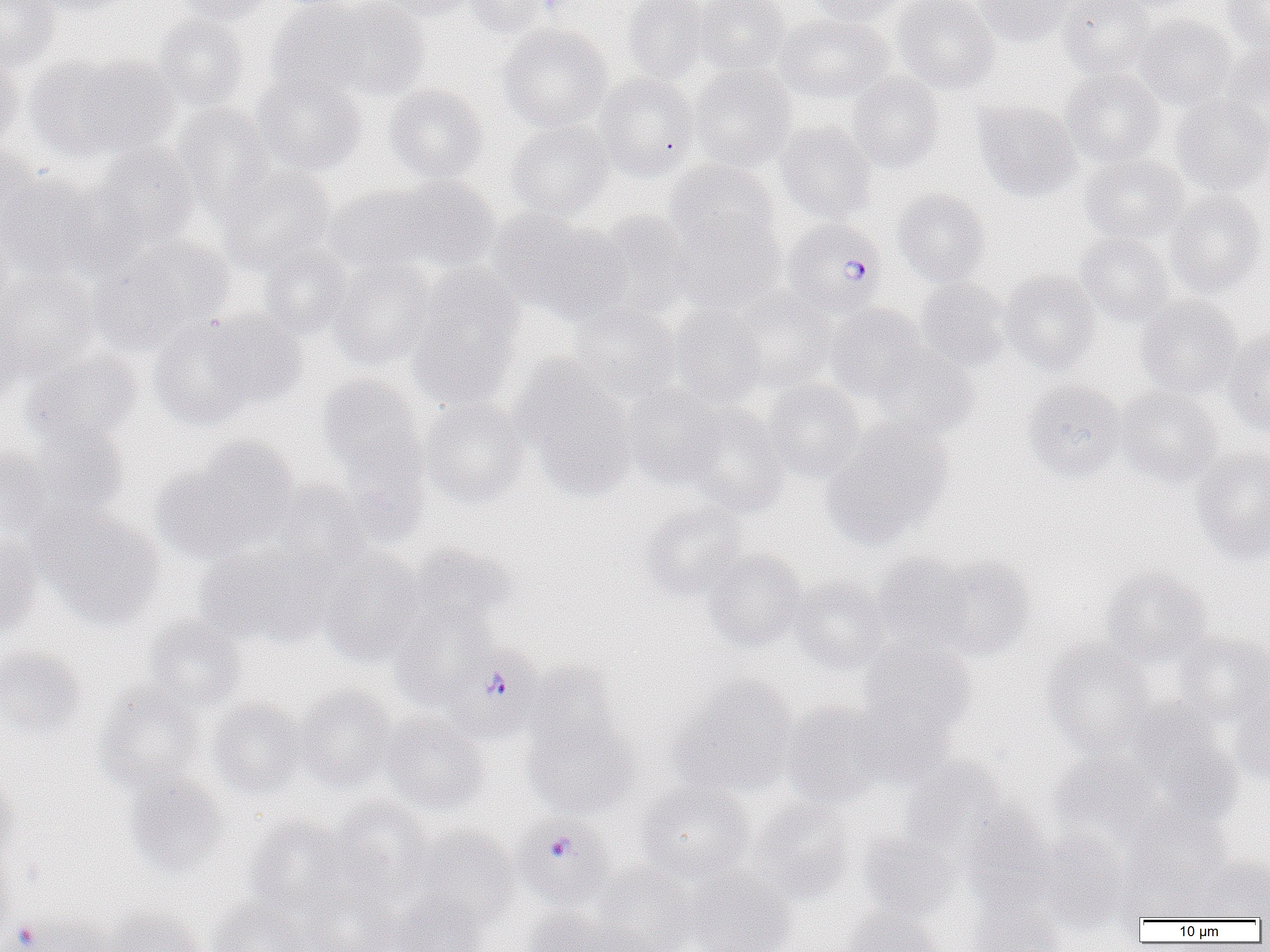
Summary:
  - Coordinate format: approximate bounding boxes as named x1/y1/x2/y2 corners in pixels
  - Plasmodium falciparum-infected red blood cell locations: (x1=782, y1=218, x2=886, y2=318), (x1=437, y1=637, x2=549, y2=743), (x1=518, y1=817, x2=610, y2=904)
  - Platelet locations: (x1=10, y1=919, x2=42, y2=951)
  - Uninfected red blood cell locations: (x1=0, y1=0, x2=61, y2=72), (x1=29, y1=0, x2=143, y2=17), (x1=173, y1=0, x2=276, y2=24), (x1=383, y1=0, x2=478, y2=20), (x1=465, y1=0, x2=555, y2=37), (x1=621, y1=0, x2=709, y2=82), (x1=694, y1=0, x2=789, y2=75), (x1=804, y1=0, x2=909, y2=24), (x1=892, y1=0, x2=1000, y2=94), (x1=973, y1=0, x2=1075, y2=47), (x1=1058, y1=0, x2=1156, y2=79), (x1=1221, y1=0, x2=1270, y2=49), (x1=266, y1=1, x2=375, y2=101), (x1=321, y1=1, x2=430, y2=102), (x1=775, y1=12, x2=892, y2=104), (x1=151, y1=14, x2=249, y2=112), (x1=1134, y1=14, x2=1237, y2=109), (x1=498, y1=23, x2=612, y2=131), (x1=1220, y1=39, x2=1270, y2=139), (x1=0, y1=53, x2=25, y2=153), (x1=39, y1=54, x2=183, y2=160), (x1=690, y1=65, x2=796, y2=171), (x1=1060, y1=69, x2=1166, y2=168), (x1=595, y1=72, x2=699, y2=180), (x1=251, y1=73, x2=368, y2=176), (x1=846, y1=73, x2=944, y2=171), (x1=383, y1=83, x2=488, y2=183), (x1=1170, y1=93, x2=1270, y2=194), (x1=973, y1=100, x2=1081, y2=201), (x1=174, y1=103, x2=276, y2=216), (x1=507, y1=120, x2=613, y2=220), (x1=775, y1=120, x2=878, y2=223), (x1=0, y1=144, x2=42, y2=237), (x1=92, y1=144, x2=199, y2=249), (x1=1079, y1=153, x2=1188, y2=244), (x1=665, y1=161, x2=779, y2=255), (x1=217, y1=165, x2=337, y2=276), (x1=0, y1=171, x2=103, y2=277), (x1=392, y1=175, x2=500, y2=272), (x1=326, y1=183, x2=442, y2=275), (x1=893, y1=188, x2=990, y2=287), (x1=1164, y1=190, x2=1268, y2=297), (x1=588, y1=210, x2=694, y2=321), (x1=670, y1=211, x2=783, y2=312), (x1=495, y1=213, x2=627, y2=321), (x1=1074, y1=231, x2=1176, y2=326), (x1=94, y1=237, x2=230, y2=348), (x1=257, y1=242, x2=354, y2=339), (x1=327, y1=259, x2=437, y2=369), (x1=0, y1=267, x2=98, y2=381), (x1=1000, y1=270, x2=1101, y2=373), (x1=407, y1=275, x2=522, y2=409), (x1=915, y1=279, x2=1011, y2=371), (x1=725, y1=289, x2=835, y2=392), (x1=1134, y1=296, x2=1242, y2=398), (x1=569, y1=303, x2=681, y2=403), (x1=667, y1=304, x2=766, y2=409), (x1=824, y1=304, x2=927, y2=400), (x1=0, y1=309, x2=23, y2=413), (x1=203, y1=309, x2=306, y2=408), (x1=148, y1=320, x2=258, y2=430), (x1=1223, y1=327, x2=1270, y2=437), (x1=872, y1=345, x2=979, y2=439), (x1=21, y1=350, x2=142, y2=452), (x1=517, y1=366, x2=638, y2=497), (x1=316, y1=374, x2=425, y2=482), (x1=763, y1=379, x2=867, y2=482), (x1=1023, y1=379, x2=1126, y2=481), (x1=622, y1=384, x2=728, y2=488), (x1=1115, y1=385, x2=1222, y2=485), (x1=420, y1=397, x2=530, y2=507), (x1=681, y1=405, x2=790, y2=517), (x1=822, y1=421, x2=952, y2=548), (x1=20, y1=424, x2=130, y2=527), (x1=156, y1=441, x2=298, y2=564), (x1=0, y1=445, x2=54, y2=538), (x1=1191, y1=447, x2=1270, y2=565), (x1=268, y1=480, x2=371, y2=577), (x1=640, y1=501, x2=748, y2=599), (x1=40, y1=511, x2=165, y2=629), (x1=0, y1=530, x2=44, y2=639), (x1=197, y1=541, x2=332, y2=647), (x1=410, y1=544, x2=516, y2=631), (x1=703, y1=548, x2=809, y2=651), (x1=318, y1=549, x2=430, y2=666), (x1=874, y1=552, x2=971, y2=646), (x1=925, y1=556, x2=1034, y2=660), (x1=1099, y1=566, x2=1211, y2=667), (x1=791, y1=574, x2=890, y2=672), (x1=391, y1=608, x2=494, y2=707), (x1=142, y1=614, x2=247, y2=712), (x1=1173, y1=631, x2=1270, y2=726), (x1=859, y1=640, x2=975, y2=739), (x1=1041, y1=641, x2=1157, y2=756), (x1=0, y1=645, x2=87, y2=743), (x1=526, y1=663, x2=622, y2=755), (x1=669, y1=675, x2=799, y2=800), (x1=95, y1=681, x2=207, y2=794), (x1=294, y1=685, x2=396, y2=791), (x1=1233, y1=693, x2=1270, y2=786), (x1=207, y1=698, x2=309, y2=799), (x1=850, y1=699, x2=957, y2=789), (x1=781, y1=701, x2=888, y2=808), (x1=1118, y1=705, x2=1241, y2=829), (x1=521, y1=708, x2=641, y2=819), (x1=378, y1=712, x2=490, y2=814), (x1=1049, y1=752, x2=1162, y2=848), (x1=902, y1=757, x2=1019, y2=862), (x1=125, y1=771, x2=230, y2=878), (x1=0, y1=772, x2=19, y2=872), (x1=637, y1=780, x2=756, y2=882), (x1=326, y1=797, x2=436, y2=902), (x1=748, y1=800, x2=857, y2=903), (x1=1127, y1=805, x2=1234, y2=901), (x1=960, y1=807, x2=1056, y2=913), (x1=245, y1=817, x2=360, y2=921), (x1=406, y1=825, x2=521, y2=928), (x1=1036, y1=829, x2=1133, y2=929), (x1=858, y1=831, x2=963, y2=924), (x1=1189, y1=854, x2=1270, y2=920), (x1=0, y1=857, x2=17, y2=949), (x1=590, y1=862, x2=697, y2=952), (x1=684, y1=866, x2=797, y2=952), (x1=295, y1=877, x2=403, y2=952), (x1=388, y1=895, x2=489, y2=952), (x1=967, y1=896, x2=1071, y2=952), (x1=208, y1=898, x2=310, y2=952), (x1=102, y1=906, x2=207, y2=952), (x1=522, y1=908, x2=624, y2=952), (x1=842, y1=909, x2=946, y2=952), (x1=16, y1=913, x2=115, y2=952)
  - Slide-level diagnosis: Plasmodium falciparum
  - Magnification: 1000x
  - Field of view: single
  - Preparation: thin blood smear
  - Image size: 1270×952 pixels
  - Modality: light microscopy